Locate every Plasmodium vivax-infected red blood cell.
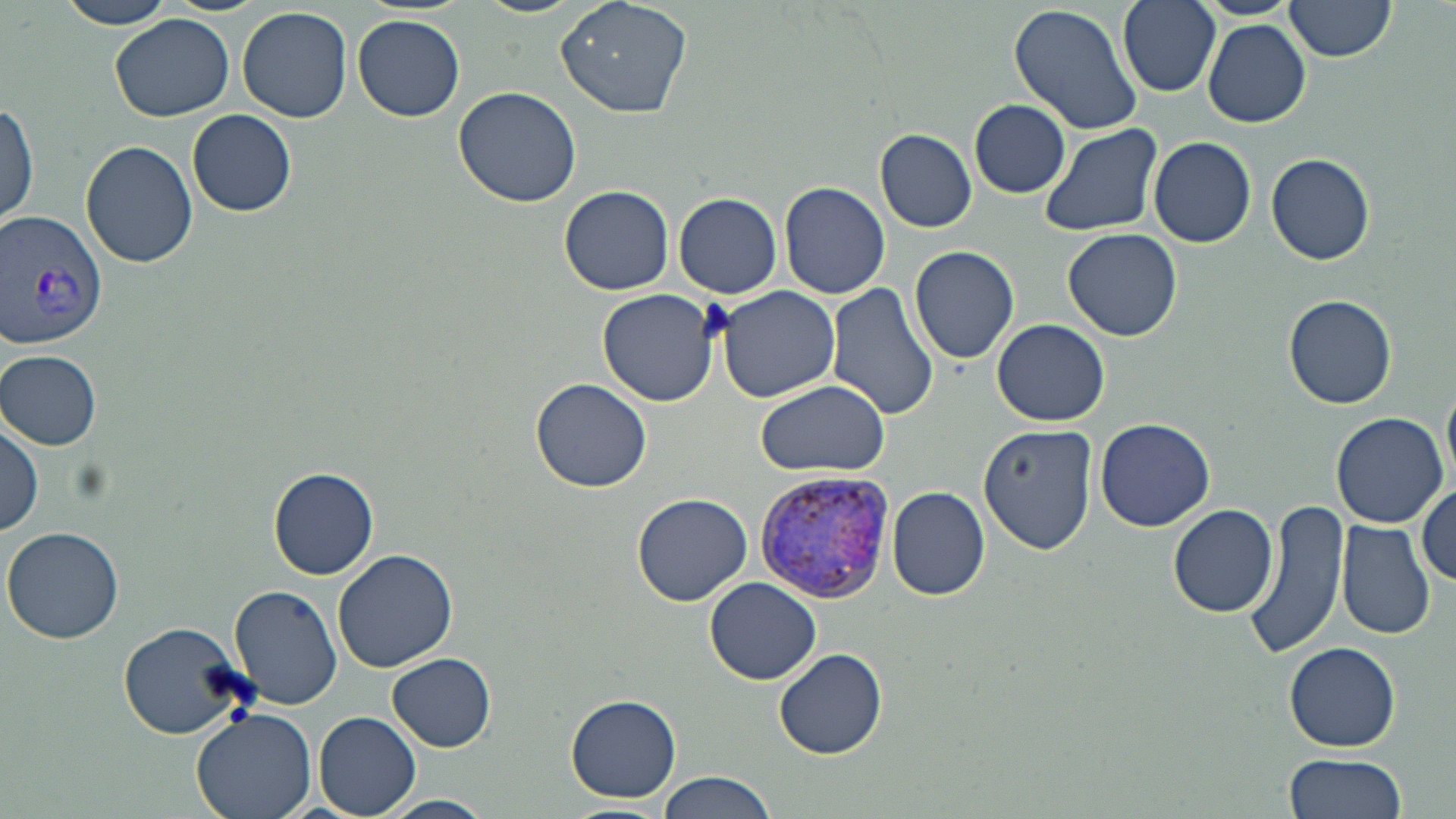
Approximate bounding boxes as (x1,y1)-(x2,y2) corner pairs in pixels.
Plasmodium vivax-infected red blood cells: (1,208)-(109,351), (756,467)-(895,607).

{
  "slide_level_diagnosis": "Plasmodium vivax",
  "platelet_locations": "approximate bounding boxes as (x1,y1)-(x2,y2) corner pairs in pixels: (696,299)-(737,343)",
  "stain": "May-Grünwald-Giemsa",
  "modality": "optical microscopy",
  "image_size": "1456×819 pixels",
  "uninfected_red_blood_cell_locations": "approximate bounding boxes as (x1,y1)-(x2,y2) corner pairs in pixels: (60,0)-(179,30), (478,0)-(586,18), (555,0)-(695,119), (1116,0)-(1222,96), (1283,1)-(1396,65), (1010,2)-(1143,138), (237,7)-(353,123), (110,14)-(240,124), (353,14)-(466,122), (1203,19)-(1312,126), (452,85)-(581,208), (969,98)-(1070,198), (0,99)-(39,231), (189,108)-(297,216), (1038,122)-(1165,239), (874,128)-(978,233), (1145,136)-(1258,249), (81,138)-(198,268), (1265,151)-(1375,267), (779,181)-(890,299), (559,183)-(676,296), (676,192)-(782,299), (1064,228)-(1182,342), (909,244)-(1019,365), (825,283)-(939,426), (714,284)-(840,402), (597,289)-(722,408), (1282,293)-(1396,409), (991,318)-(1110,426), (1,350)-(102,448), (530,376)-(652,492), (1444,379)-(1456,486), (756,380)-(889,478), (1330,412)-(1450,528), (1094,417)-(1216,532), (1,419)-(43,537), (978,423)-(1099,554), (269,466)-(380,579), (1414,483)-(1454,586), (887,486)-(990,600), (630,494)-(754,607), (1242,498)-(1349,662), (1168,504)-(1280,617), (1336,519)-(1436,641), (3,526)-(125,642), (332,549)-(458,674), (705,577)-(822,685), (229,583)-(342,712), (119,618)-(250,740), (1284,642)-(1402,751), (775,647)-(888,759), (388,653)-(496,750), (566,693)-(682,803), (190,708)-(316,819), (315,712)-(421,818), (1281,753)-(1408,819), (657,772)-(779,819), (385,795)-(493,818), (556,802)-(670,819)",
  "preparation": "thin blood film",
  "magnification": "1000x",
  "field_of_view": "one of a larger specimen"
}